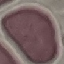 Result: no malaria parasites detected. Photographed with a smartphone camera at the microscope eyepiece. Thin blood smear. Cell patch, automatically extracted from a larger field of view and resized to 64 × 64 pixels. Giemsa stain.